Give the position of every Plasmodium parasite.
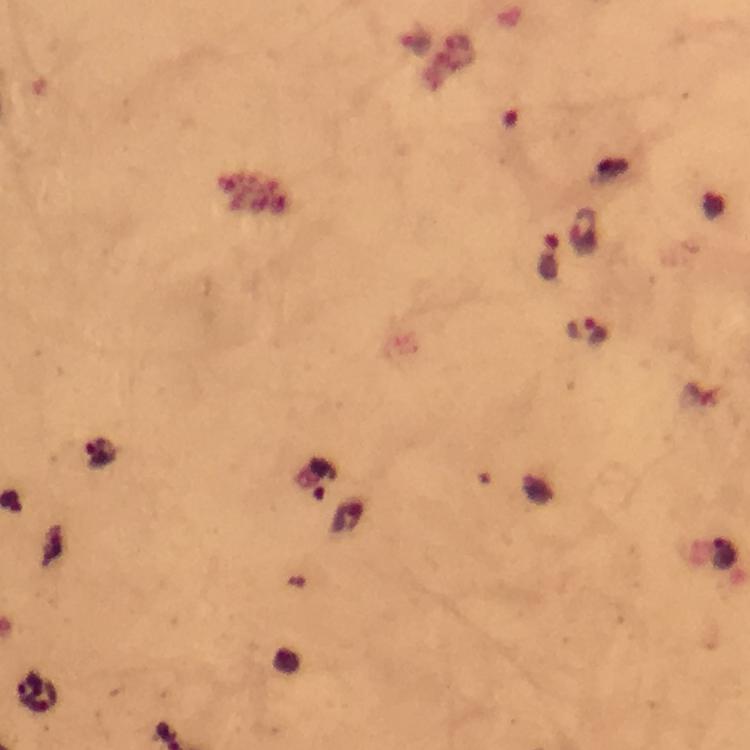

Approximate centers as (x, y) in pixels.
Plasmodium parasites: (584, 233), (550, 257), (589, 330), (101, 453).

magnification = 100x
stain = Giemsa
preparation = thick smear
context = from a malaria diagnostic workup
cropped from = one field of view
image size = 750×750 pixels
capture = smartphone photograph through a microscope
immersion oil = used